Locate every Plasmodium parasite and every leukocyte.
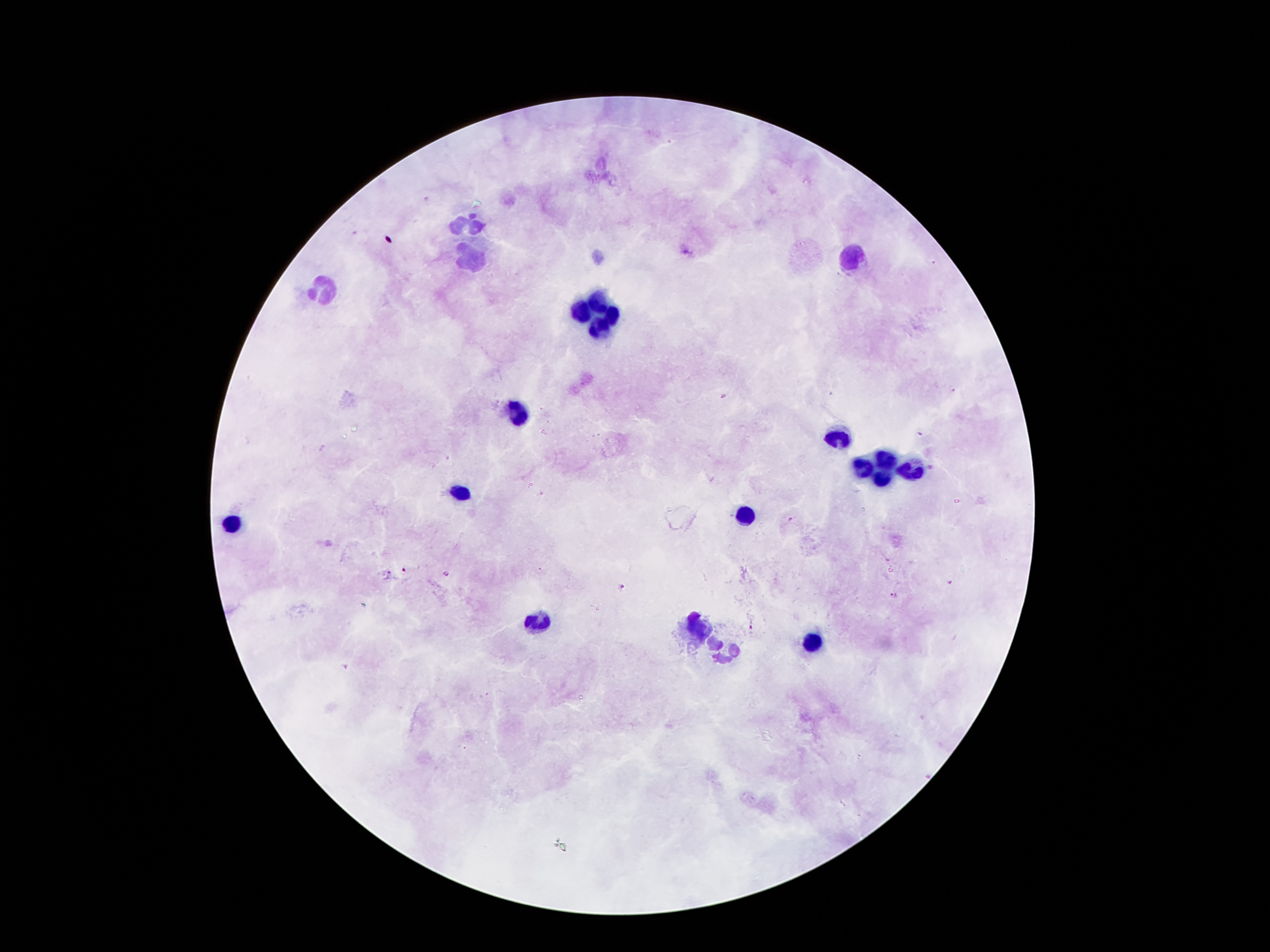

Approximate centers as {x, y} in pixels.
Plasmodium parasites: {951, 389}, {725, 397}, {920, 434}, {791, 519}, {403, 570}, {389, 573}, {447, 574}, {950, 582}, {621, 588}, {893, 595}, {752, 629}, {345, 666}.
Leukocytes: {473, 224}, {470, 255}, {855, 257}, {323, 294}, {601, 304}, {584, 310}, {612, 315}, {599, 327}, {517, 413}, {836, 439}, {885, 460}, {862, 469}, {909, 471}, {879, 479}, {461, 492}, {746, 513}, {233, 525}, {535, 625}, {699, 628}, {809, 642}, {727, 649}.

Thick blood smear. 100x magnification. Patient malaria status: positive for Plasmodium falciparum. Single field of view. Smartphone photograph taken through the microscope eyepiece. Image is 1270×952 pixels. Giemsa-stained preparation.